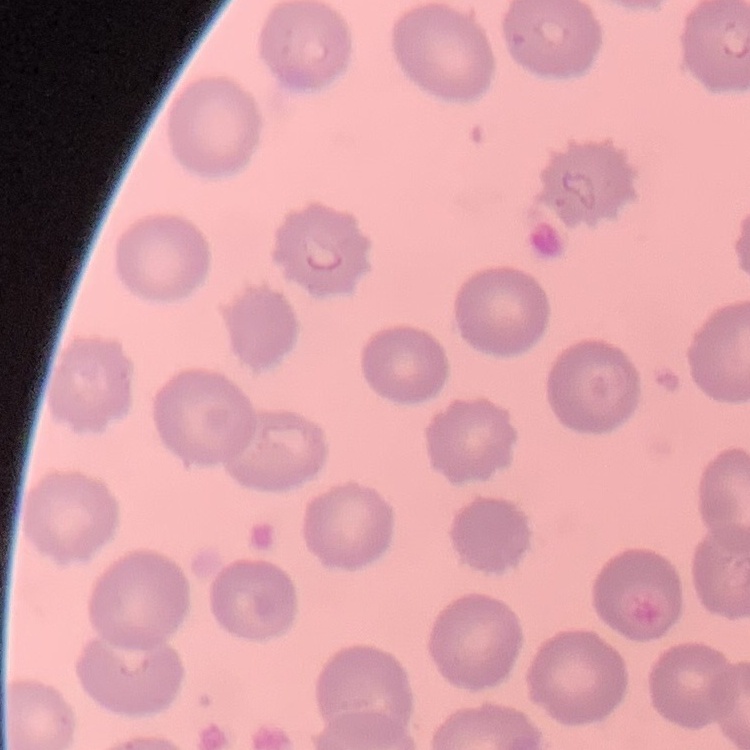
The red blood cells show no rouleaux formation. Thin blood film. One tile cut from a larger photomicrograph. Field's or Giemsa stain.